Assess the morphology of the erythrocytes.
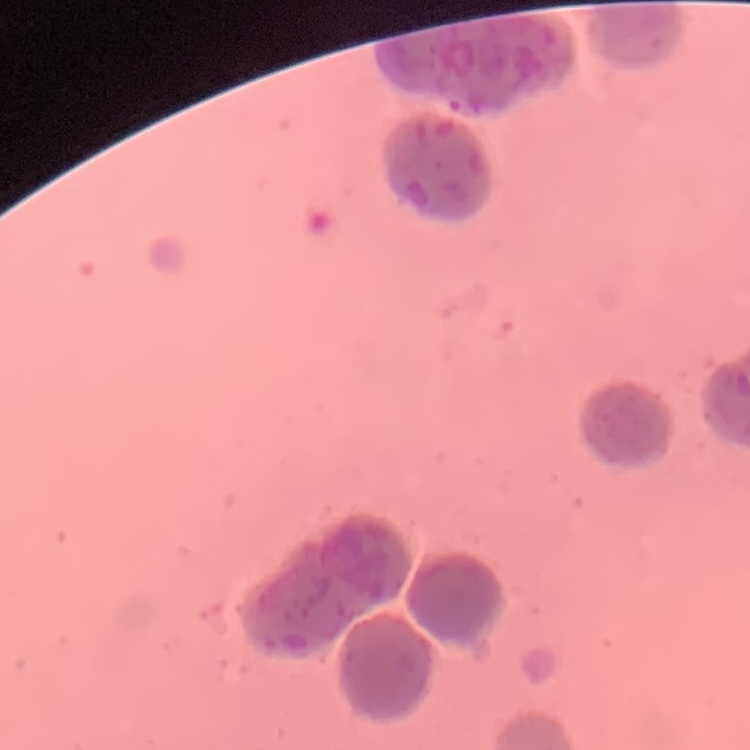
They show rouleaux formation.

Summary:
  - Image type: square crop of a larger photomicrograph
  - Preparation: thin peripheral smear
  - Stain: Field's or Giemsa